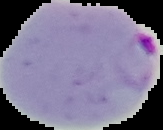

preparation = thin blood smear
image size = 163×130 pixels
image type = segmented cell region on a black background
result = malaria parasites detected